Identify the parasite.
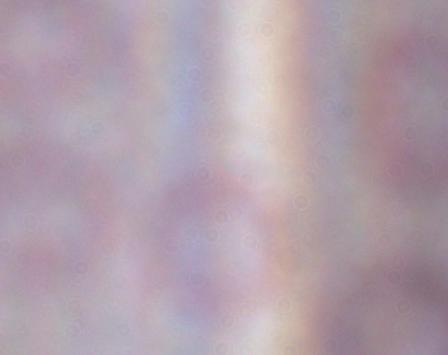

A trypanosome.

magnification: 1000x
modality: micrograph